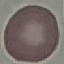
Summary:
  - Result: no malaria parasites detected
  - Image type: automatically extracted cell patch, resized to 64 × 64 pixels
  - Capture: smartphone camera at the microscope eyepiece
  - Preparation: thin blood smear
  - Stain: Giemsa